Report the malaria status of this cell.
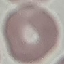
It is uninfected.

Thin blood film. Giemsa stain. Photographed with a smartphone camera at the microscope eyepiece. Cell patch, automatically extracted from a larger field of view and resized to 64 × 64 pixels.